Outline each Plasmodium falciparum-infected red blood cell.
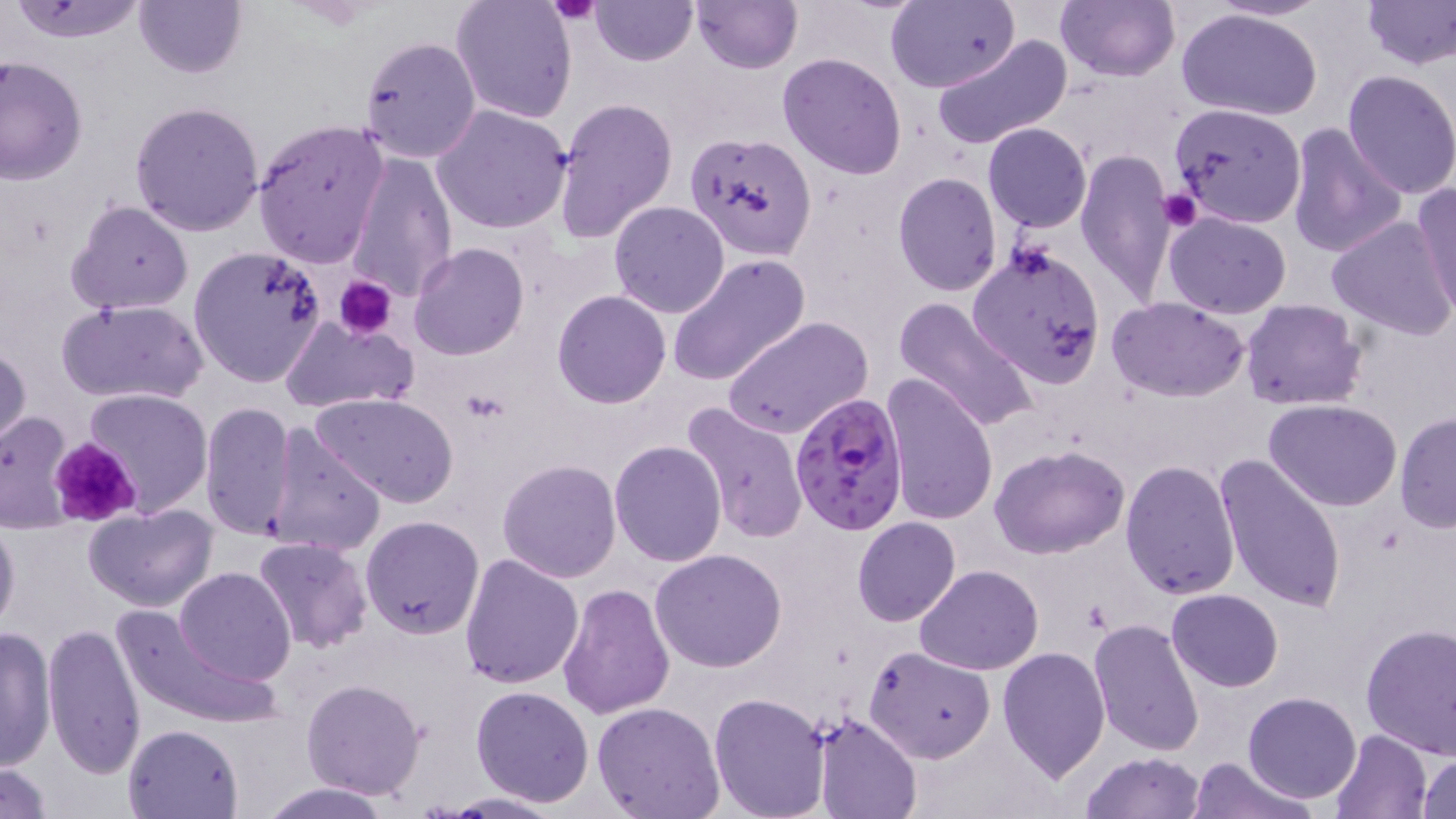
Approximate bounding boxes as named x1/y1/x2/y2 corners in pixels.
Plasmodium falciparum-infected red blood cells: (x1=788, y1=391, x2=908, y2=533).

Summary:
  - Uninfected red blood cell locations: (x1=4, y1=0, x2=154, y2=44), (x1=589, y1=0, x2=698, y2=66), (x1=689, y1=0, x2=801, y2=73), (x1=887, y1=0, x2=1020, y2=93), (x1=1056, y1=0, x2=1179, y2=82), (x1=133, y1=1, x2=248, y2=79), (x1=450, y1=1, x2=579, y2=125), (x1=1362, y1=1, x2=1456, y2=70), (x1=1175, y1=7, x2=1324, y2=123), (x1=358, y1=35, x2=483, y2=164), (x1=930, y1=35, x2=1073, y2=150), (x1=777, y1=52, x2=907, y2=179), (x1=0, y1=56, x2=87, y2=187), (x1=1342, y1=70, x2=1456, y2=199), (x1=552, y1=94, x2=679, y2=243), (x1=128, y1=100, x2=265, y2=236), (x1=1168, y1=102, x2=1307, y2=228), (x1=432, y1=104, x2=572, y2=234), (x1=251, y1=119, x2=389, y2=268), (x1=983, y1=122, x2=1092, y2=232), (x1=1286, y1=124, x2=1405, y2=259), (x1=687, y1=136, x2=814, y2=264), (x1=1076, y1=148, x2=1176, y2=307), (x1=344, y1=152, x2=457, y2=301), (x1=892, y1=172, x2=1003, y2=295), (x1=1410, y1=184, x2=1456, y2=314), (x1=67, y1=199, x2=194, y2=316), (x1=607, y1=201, x2=729, y2=319), (x1=1163, y1=210, x2=1291, y2=317), (x1=1327, y1=215, x2=1456, y2=339), (x1=409, y1=244, x2=529, y2=362), (x1=966, y1=244, x2=1105, y2=388), (x1=188, y1=246, x2=329, y2=388), (x1=667, y1=253, x2=810, y2=387), (x1=552, y1=290, x2=672, y2=409), (x1=894, y1=297, x2=1041, y2=435), (x1=1107, y1=297, x2=1250, y2=401), (x1=57, y1=298, x2=208, y2=405), (x1=1240, y1=299, x2=1368, y2=410), (x1=722, y1=315, x2=873, y2=441), (x1=278, y1=316, x2=418, y2=415), (x1=0, y1=341, x2=31, y2=456), (x1=881, y1=372, x2=1000, y2=526), (x1=81, y1=387, x2=213, y2=518), (x1=312, y1=392, x2=459, y2=506), (x1=1265, y1=398, x2=1403, y2=511), (x1=198, y1=401, x2=298, y2=544), (x1=681, y1=402, x2=808, y2=544), (x1=0, y1=410, x2=75, y2=534), (x1=1394, y1=413, x2=1455, y2=534), (x1=260, y1=424, x2=387, y2=558), (x1=609, y1=441, x2=726, y2=567), (x1=991, y1=445, x2=1131, y2=558), (x1=1213, y1=452, x2=1347, y2=615), (x1=496, y1=458, x2=622, y2=582), (x1=1120, y1=459, x2=1240, y2=600), (x1=84, y1=503, x2=222, y2=613), (x1=0, y1=509, x2=20, y2=640), (x1=360, y1=515, x2=485, y2=640), (x1=852, y1=516, x2=960, y2=626), (x1=252, y1=537, x2=373, y2=653), (x1=649, y1=549, x2=788, y2=672), (x1=458, y1=552, x2=583, y2=688), (x1=174, y1=566, x2=298, y2=685), (x1=914, y1=566, x2=1041, y2=676), (x1=556, y1=581, x2=674, y2=722), (x1=1167, y1=588, x2=1284, y2=691), (x1=110, y1=602, x2=278, y2=730), (x1=1088, y1=618, x2=1205, y2=759), (x1=43, y1=620, x2=145, y2=777), (x1=1360, y1=623, x2=1456, y2=757), (x1=0, y1=626, x2=57, y2=773), (x1=865, y1=645, x2=996, y2=762), (x1=997, y1=646, x2=1111, y2=781), (x1=301, y1=677, x2=426, y2=801), (x1=470, y1=685, x2=596, y2=806), (x1=709, y1=692, x2=830, y2=819), (x1=1244, y1=692, x2=1361, y2=802), (x1=592, y1=701, x2=725, y2=819), (x1=811, y1=714, x2=922, y2=819), (x1=123, y1=723, x2=243, y2=818), (x1=1328, y1=730, x2=1432, y2=819), (x1=1080, y1=752, x2=1205, y2=819), (x1=1417, y1=752, x2=1455, y2=817), (x1=1192, y1=756, x2=1310, y2=819), (x1=0, y1=762, x2=53, y2=817), (x1=259, y1=782, x2=396, y2=818), (x1=442, y1=792, x2=565, y2=818)
  - Platelet locations: (x1=550, y1=0, x2=600, y2=25), (x1=1157, y1=187, x2=1202, y2=233), (x1=334, y1=275, x2=397, y2=339), (x1=51, y1=435, x2=143, y2=528)
  - Slide-level diagnosis: Plasmodium falciparum
  - Modality: light microscopy
  - Magnification: 1000x
  - Stain: May-Grünwald-Giemsa
  - Image size: 1456×819 pixels
  - Preparation: thin blood smear
  - Field of view: single